Give the preparation type.
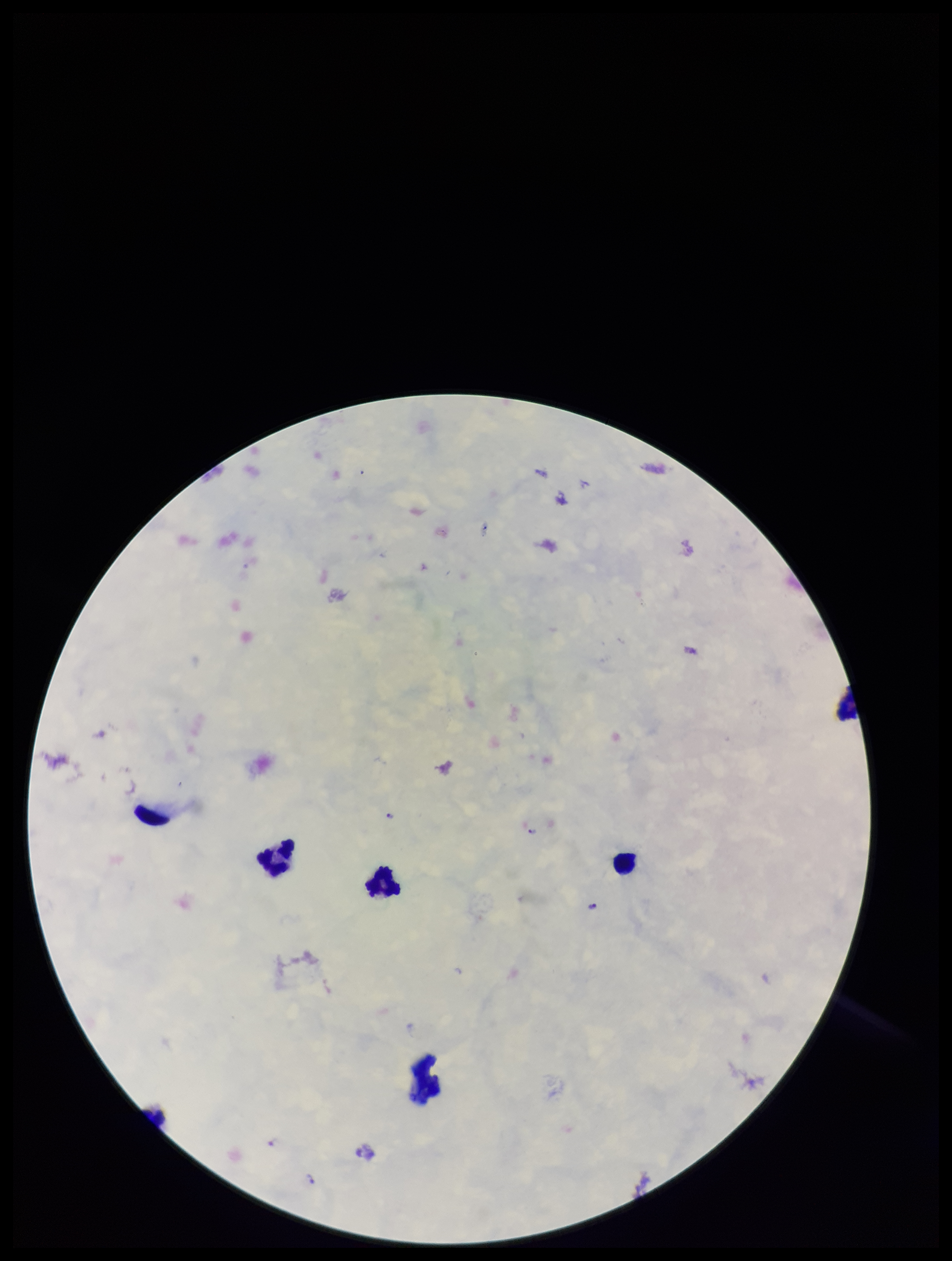

Thick.

Summary:
  - Image size: 952×1261 pixels
  - Patient malaria status: infected
  - Capture: smartphone photograph through the microscope eyepiece
  - Parasite count: 6
  - Plasmodium parasites: detected
  - Leukocyte count: 5
  - Field of view: single
  - Stain: Giemsa
  - Species reported for this patient: Plasmodium falciparum